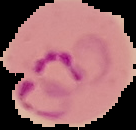

preparation: thin blood film
result: malaria parasites detected
image_size: 136×130 pixels
image_type: segmented cell region on a black background